Identify the blood parasite species.
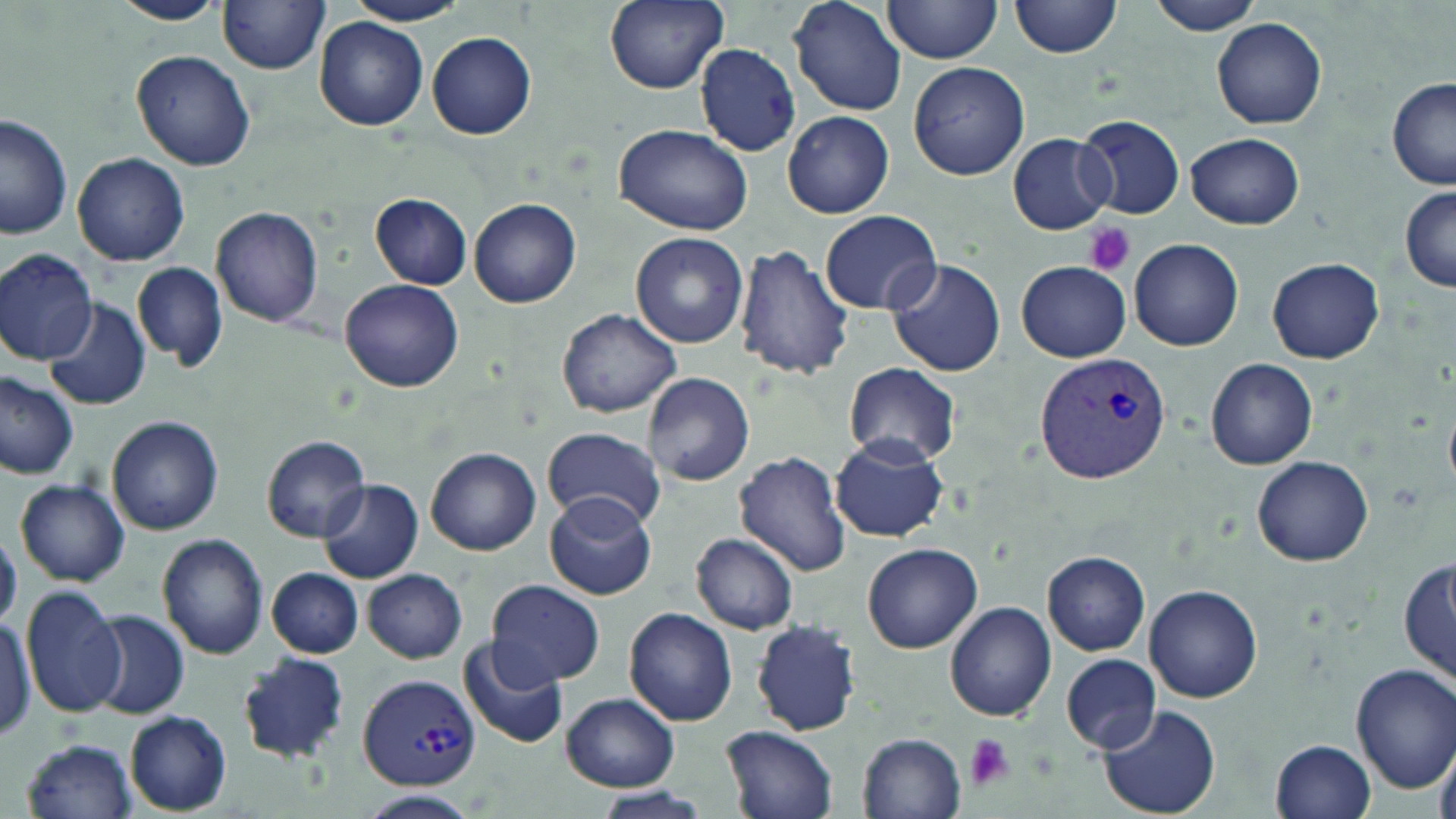

Plasmodium vivax.

Summary:
  - Coordinate format: approximate bounding boxes as named x1/y1/x2/y2 corners in pixels
  - Platelet locations: (x1=1082, y1=223, x2=1137, y2=276), (x1=964, y1=735, x2=1013, y2=790)
  - Uninfected red blood cell locations: (x1=345, y1=0, x2=469, y2=26), (x1=604, y1=0, x2=728, y2=92), (x1=788, y1=0, x2=908, y2=117), (x1=882, y1=0, x2=1005, y2=63), (x1=1146, y1=0, x2=1268, y2=36), (x1=111, y1=1, x2=225, y2=25), (x1=219, y1=1, x2=331, y2=74), (x1=1008, y1=1, x2=1122, y2=61), (x1=314, y1=17, x2=429, y2=130), (x1=1212, y1=17, x2=1327, y2=128), (x1=425, y1=31, x2=536, y2=140), (x1=695, y1=43, x2=801, y2=157), (x1=130, y1=49, x2=256, y2=172), (x1=909, y1=63, x2=1029, y2=181), (x1=1387, y1=76, x2=1456, y2=190), (x1=782, y1=109, x2=894, y2=219), (x1=1, y1=113, x2=73, y2=241), (x1=1074, y1=113, x2=1187, y2=220), (x1=613, y1=122, x2=754, y2=236), (x1=1008, y1=132, x2=1115, y2=234), (x1=1187, y1=132, x2=1304, y2=230), (x1=73, y1=151, x2=189, y2=266), (x1=1400, y1=186, x2=1456, y2=291), (x1=371, y1=193, x2=472, y2=289), (x1=468, y1=196, x2=582, y2=308), (x1=211, y1=207, x2=324, y2=328), (x1=819, y1=210, x2=942, y2=315), (x1=631, y1=232, x2=748, y2=349), (x1=1129, y1=239, x2=1245, y2=350), (x1=732, y1=245, x2=854, y2=380), (x1=1, y1=249, x2=99, y2=364), (x1=1266, y1=256, x2=1384, y2=364), (x1=886, y1=258, x2=1007, y2=378), (x1=1015, y1=260, x2=1131, y2=362), (x1=134, y1=262, x2=228, y2=371), (x1=339, y1=278, x2=466, y2=392), (x1=42, y1=296, x2=149, y2=411), (x1=555, y1=307, x2=681, y2=418), (x1=1207, y1=358, x2=1319, y2=469), (x1=844, y1=362, x2=960, y2=468), (x1=643, y1=372, x2=754, y2=487), (x1=0, y1=373, x2=79, y2=479), (x1=107, y1=416, x2=225, y2=537), (x1=542, y1=427, x2=664, y2=529), (x1=261, y1=434, x2=372, y2=543), (x1=830, y1=434, x2=949, y2=542), (x1=425, y1=447, x2=542, y2=555), (x1=733, y1=450, x2=851, y2=576), (x1=1251, y1=456, x2=1375, y2=567), (x1=15, y1=477, x2=129, y2=587), (x1=320, y1=478, x2=423, y2=584), (x1=543, y1=491, x2=659, y2=601), (x1=1, y1=530, x2=22, y2=630), (x1=156, y1=533, x2=268, y2=660), (x1=691, y1=533, x2=800, y2=635), (x1=861, y1=543, x2=982, y2=654), (x1=1042, y1=551, x2=1150, y2=655), (x1=1398, y1=554, x2=1455, y2=688), (x1=267, y1=567, x2=363, y2=659), (x1=362, y1=568, x2=468, y2=663), (x1=485, y1=580, x2=605, y2=688), (x1=1144, y1=583, x2=1263, y2=702), (x1=21, y1=586, x2=127, y2=718), (x1=944, y1=602, x2=1057, y2=721), (x1=625, y1=607, x2=738, y2=726), (x1=88, y1=610, x2=188, y2=720), (x1=751, y1=618, x2=862, y2=736), (x1=458, y1=636, x2=572, y2=751), (x1=235, y1=654, x2=352, y2=765), (x1=1062, y1=655, x2=1161, y2=754), (x1=1352, y1=663, x2=1456, y2=795), (x1=560, y1=693, x2=680, y2=792), (x1=1097, y1=704, x2=1222, y2=819), (x1=126, y1=711, x2=232, y2=815), (x1=720, y1=725, x2=840, y2=819), (x1=858, y1=733, x2=967, y2=819), (x1=20, y1=737, x2=138, y2=819), (x1=1269, y1=740, x2=1376, y2=819), (x1=591, y1=786, x2=716, y2=818), (x1=355, y1=790, x2=481, y2=819)
  - Plasmodium vivax-infected red blood cell locations: (x1=1036, y1=353, x2=1171, y2=482), (x1=357, y1=672, x2=480, y2=790)
  - Image size: 1456×819 pixels
  - Magnification: 1000x
  - Stain: May-Grünwald-Giemsa
  - Field of view: single
  - Preparation: thin blood film
  - Modality: light microscopy